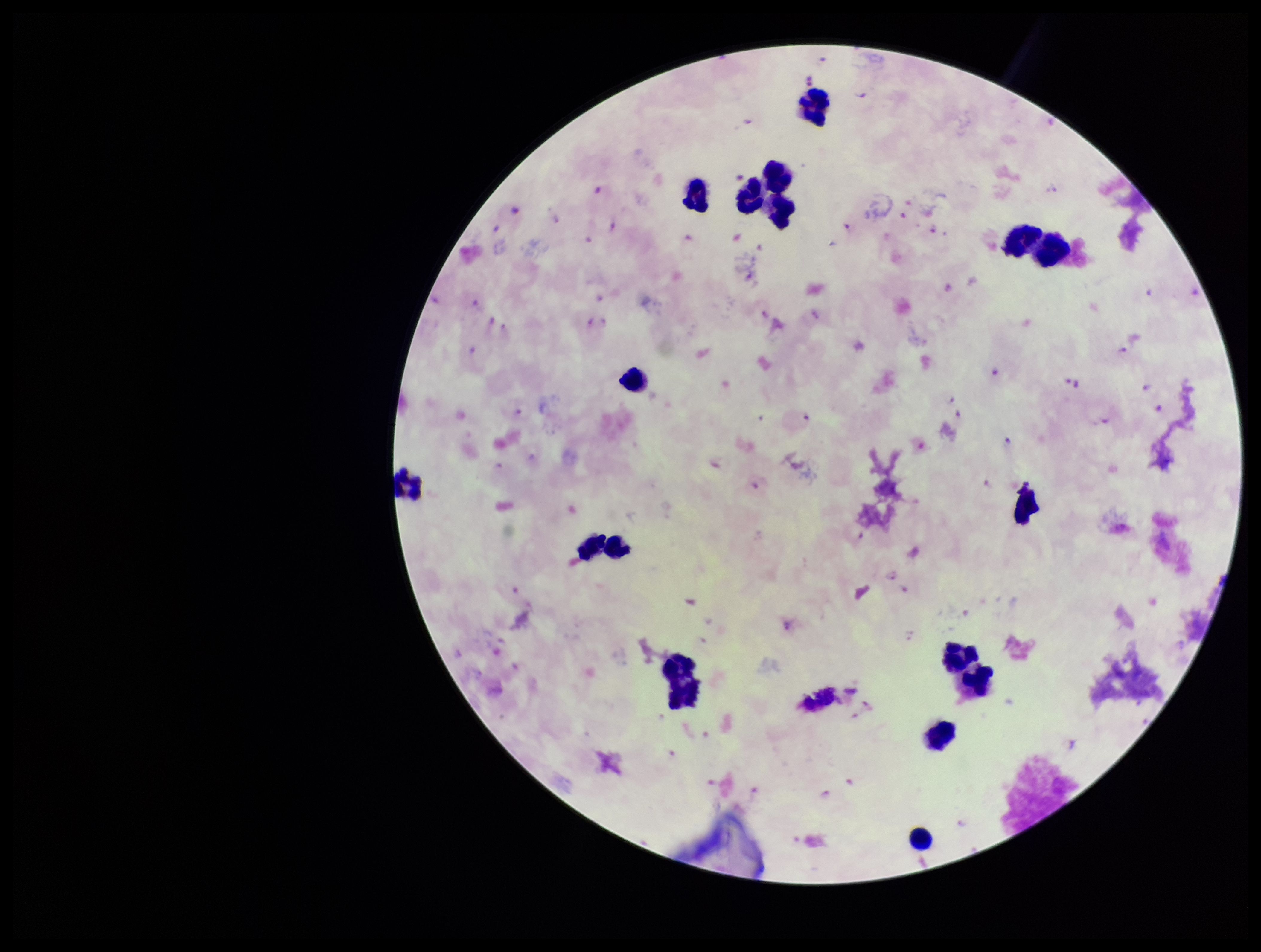
leukocyte count = 15
field of view = one from this slide
preparation = thick smear
patient malaria status = infected
stain = Giemsa
image size = 1261×952 pixels
Plasmodium parasites = seen
capture = smartphone photograph through the microscope eyepiece
species reported for this patient = Plasmodium falciparum
parasite count = 52